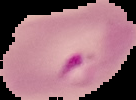

Summary:
  - Result: malaria parasites identified
  - Preparation: thin blood film
  - Image type: segmented cell region on a black background
  - Image size: 136×100 pixels